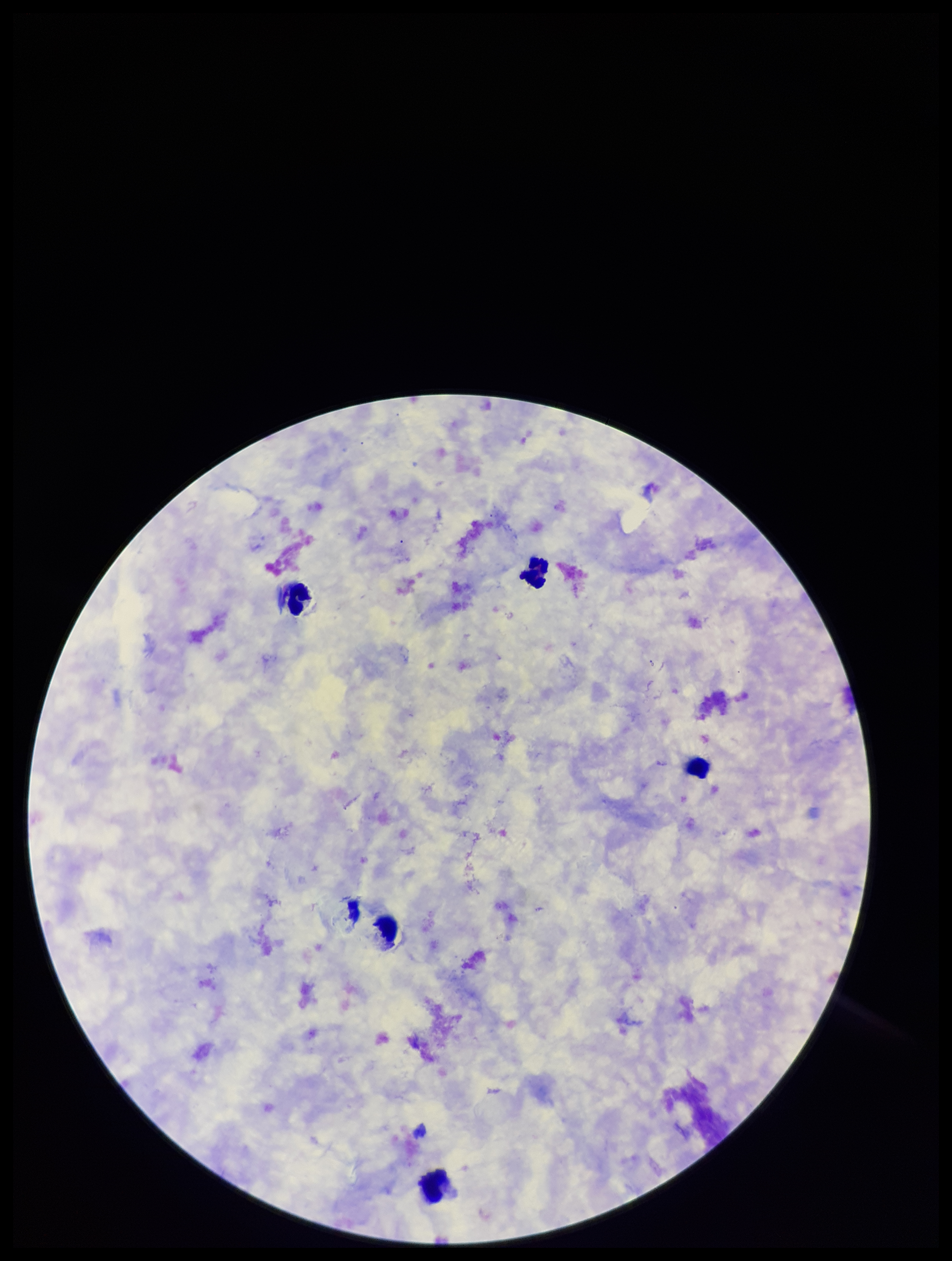
Summary:
  - Plasmodium parasites: none detected
  - Stain: Giemsa
  - Preparation: thick blood smear
  - Field of view: single
  - Capture: smartphone photograph through the microscope eyepiece
  - Leukocyte count: 5
  - Patient malaria status: negative
  - Image size: 952×1261 pixels
  - Parasite count: 0